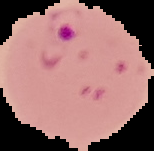

result = malaria parasites identified
image size = 154×151 pixels
image type = segmented cell region on a black background
preparation = thin blood film